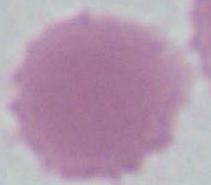
identification = erythrocyte
modality = micrograph
magnification = 1000x